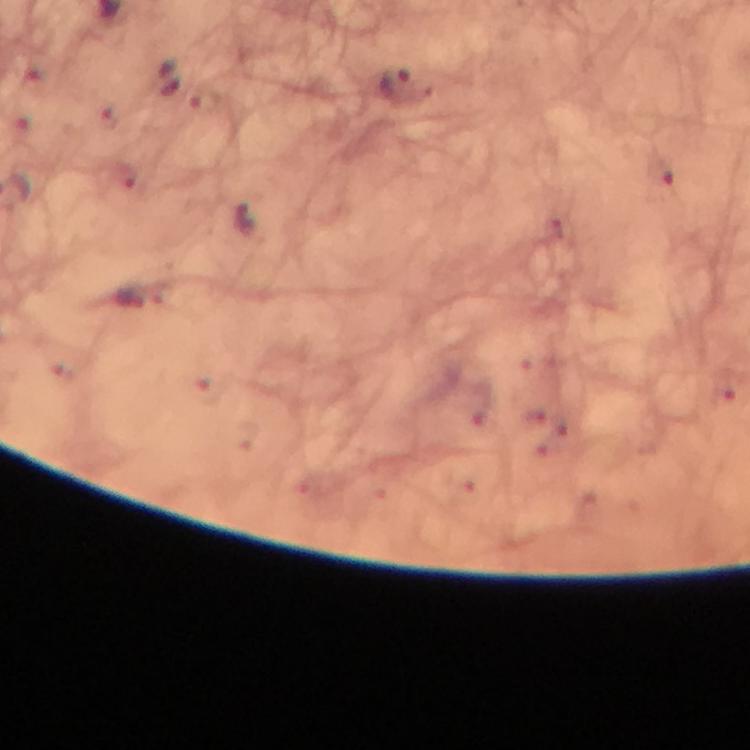

image size = 750×750 pixels
malaria parasite locations = approximate centers as {x, y} in pixels: {397, 82}, {661, 169}
magnification = 100x
immersion oil = used
preparation = thick blood smear
context = from a diagnostic examination for malaria
stain = Giemsa
capture = smartphone camera through the microscope
cropped from = one field of view